Outline each blood parasite and name the species.
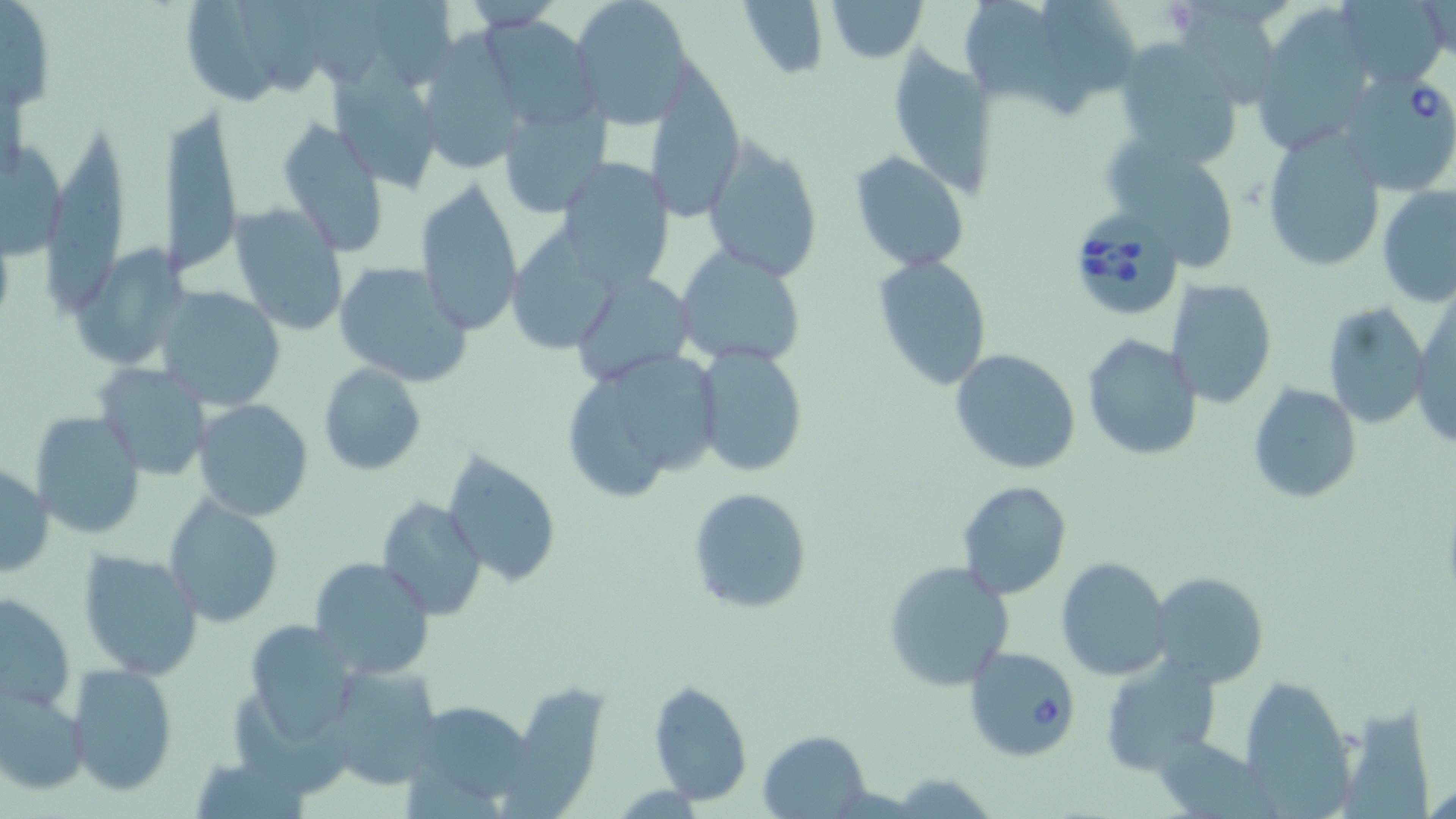
Approximate bounding boxes as named x1/y1/x2/y2 corners in pixels.
Babesia divergens-infected red blood cells: (x1=1337, y1=73, x2=1456, y2=196), (x1=1064, y1=205, x2=1189, y2=314), (x1=962, y1=646, x2=1080, y2=761).
No Plasmodium falciparum, Plasmodium ovale, Plasmodium malariae, Plasmodium vivax, or Trypanosoma brucei observed.

slide-level diagnosis = Babesia divergens
image size = 1456×819 pixels
modality = light microscopy
field of view = single
preparation = thin blood smear
uninfected red blood cell locations = approximate bounding boxes as named x1/y1/x2/y2 corners in pixels: (x1=184, y1=0, x2=279, y2=111), (x1=243, y1=0, x2=324, y2=95), (x1=305, y1=0, x2=382, y2=85), (x1=569, y1=0, x2=698, y2=126), (x1=744, y1=0, x2=827, y2=83), (x1=824, y1=0, x2=928, y2=61), (x1=966, y1=0, x2=1078, y2=117), (x1=1044, y1=0, x2=1134, y2=94), (x1=1341, y1=1, x2=1449, y2=89), (x1=1, y1=2, x2=58, y2=114), (x1=1179, y1=6, x2=1284, y2=104), (x1=1261, y1=11, x2=1370, y2=150), (x1=478, y1=17, x2=598, y2=131), (x1=413, y1=36, x2=530, y2=175), (x1=1110, y1=39, x2=1249, y2=168), (x1=889, y1=50, x2=998, y2=198), (x1=331, y1=65, x2=444, y2=193), (x1=646, y1=68, x2=746, y2=221), (x1=498, y1=100, x2=612, y2=218), (x1=159, y1=107, x2=242, y2=277), (x1=278, y1=117, x2=390, y2=258), (x1=1261, y1=130, x2=1387, y2=272), (x1=0, y1=136, x2=65, y2=263), (x1=47, y1=136, x2=126, y2=315), (x1=699, y1=137, x2=824, y2=283), (x1=1110, y1=143, x2=1234, y2=271), (x1=849, y1=151, x2=970, y2=272), (x1=554, y1=156, x2=677, y2=290), (x1=413, y1=176, x2=524, y2=336), (x1=1378, y1=184, x2=1456, y2=307), (x1=228, y1=203, x2=348, y2=336), (x1=505, y1=228, x2=624, y2=353), (x1=70, y1=244, x2=190, y2=372), (x1=674, y1=246, x2=808, y2=367), (x1=872, y1=256, x2=992, y2=391), (x1=332, y1=260, x2=476, y2=388), (x1=571, y1=271, x2=696, y2=384), (x1=1165, y1=278, x2=1278, y2=409), (x1=153, y1=286, x2=287, y2=411), (x1=1412, y1=297, x2=1456, y2=452), (x1=1321, y1=302, x2=1427, y2=431), (x1=1081, y1=332, x2=1203, y2=459), (x1=693, y1=345, x2=808, y2=479), (x1=949, y1=348, x2=1081, y2=475), (x1=622, y1=351, x2=717, y2=472), (x1=95, y1=362, x2=212, y2=481), (x1=318, y1=364, x2=425, y2=477), (x1=575, y1=376, x2=666, y2=499), (x1=1247, y1=381, x2=1361, y2=504), (x1=191, y1=399, x2=314, y2=521), (x1=30, y1=411, x2=148, y2=540), (x1=443, y1=451, x2=560, y2=586), (x1=0, y1=464, x2=52, y2=578), (x1=956, y1=481, x2=1072, y2=600), (x1=687, y1=487, x2=813, y2=614), (x1=163, y1=494, x2=284, y2=628), (x1=376, y1=497, x2=487, y2=620), (x1=75, y1=548, x2=204, y2=681), (x1=309, y1=557, x2=436, y2=678), (x1=1056, y1=557, x2=1174, y2=681), (x1=882, y1=560, x2=1016, y2=691), (x1=1149, y1=571, x2=1269, y2=687), (x1=1, y1=591, x2=76, y2=714), (x1=241, y1=620, x2=357, y2=742), (x1=1098, y1=655, x2=1221, y2=776), (x1=66, y1=664, x2=177, y2=796), (x1=319, y1=664, x2=447, y2=792), (x1=1241, y1=676, x2=1354, y2=812), (x1=649, y1=681, x2=753, y2=807), (x1=0, y1=685, x2=90, y2=797), (x1=502, y1=686, x2=609, y2=819), (x1=232, y1=690, x2=348, y2=790), (x1=426, y1=704, x2=540, y2=800), (x1=1345, y1=705, x2=1437, y2=819), (x1=1156, y1=728, x2=1295, y2=819), (x1=759, y1=729, x2=869, y2=816), (x1=201, y1=761, x2=310, y2=819), (x1=890, y1=770, x2=998, y2=818)
magnification = 1000x
stain = May-Grünwald-Giemsa